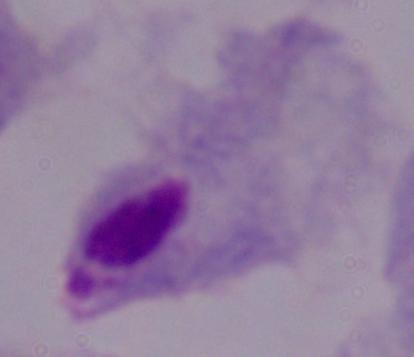
1000x magnification. Photomicrograph. A trichomonad is shown.